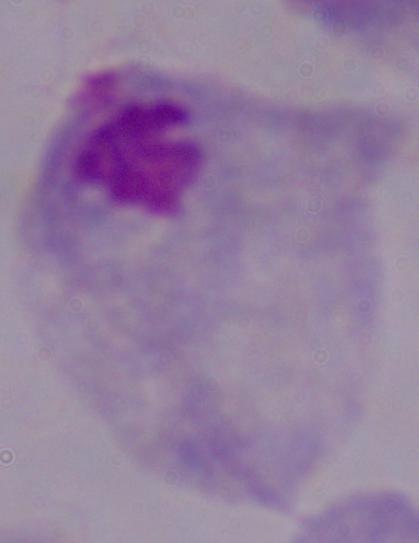
modality = micrograph
magnification = 1000x
identification = trichomonad